Evaluate for malaria.
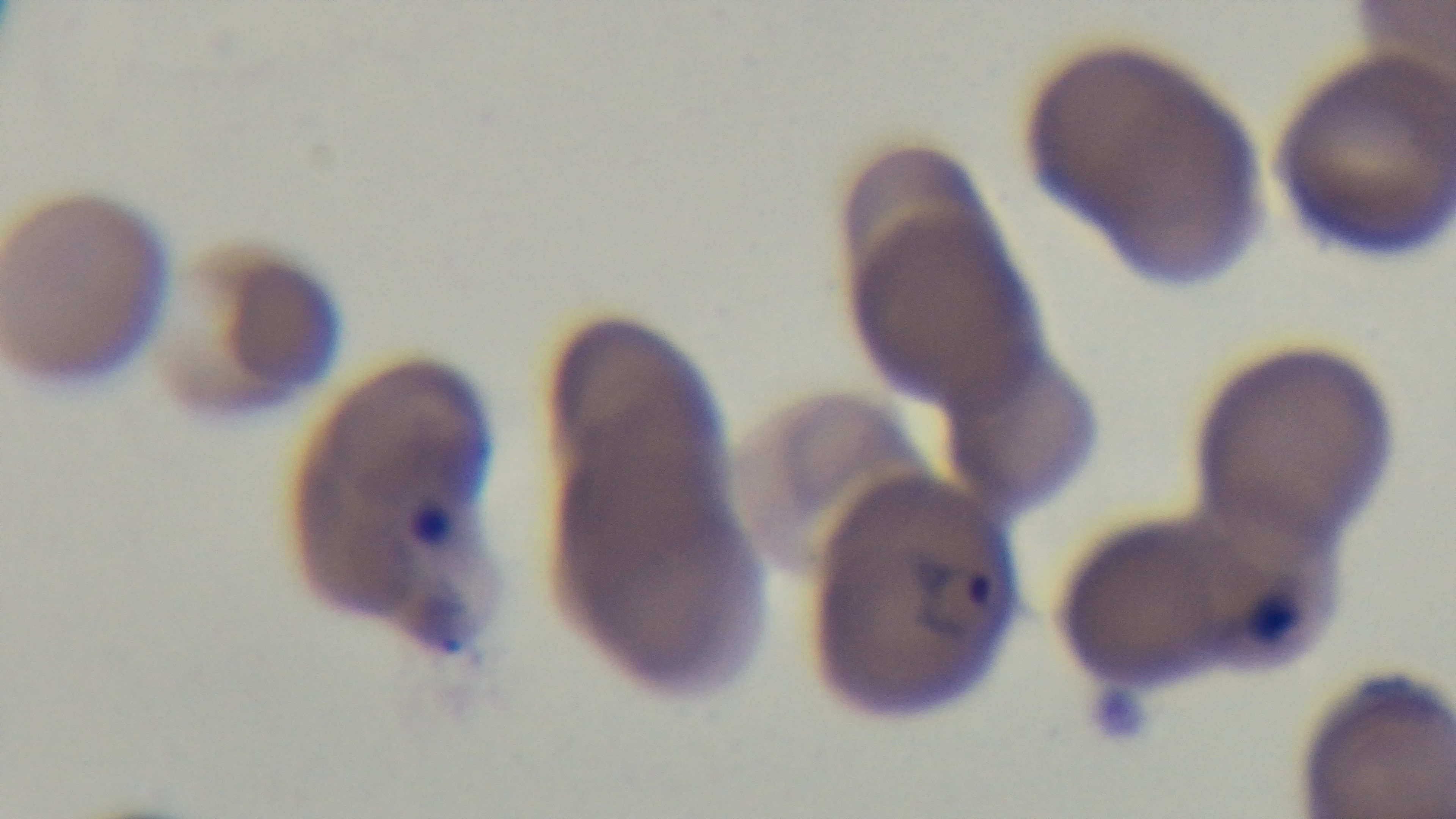

Positive.

stain = Giemsa
objective = 100x oil immersion
modality = light microscopy
capture = mounted 4K digital camera
preparation = thin
field of view = single